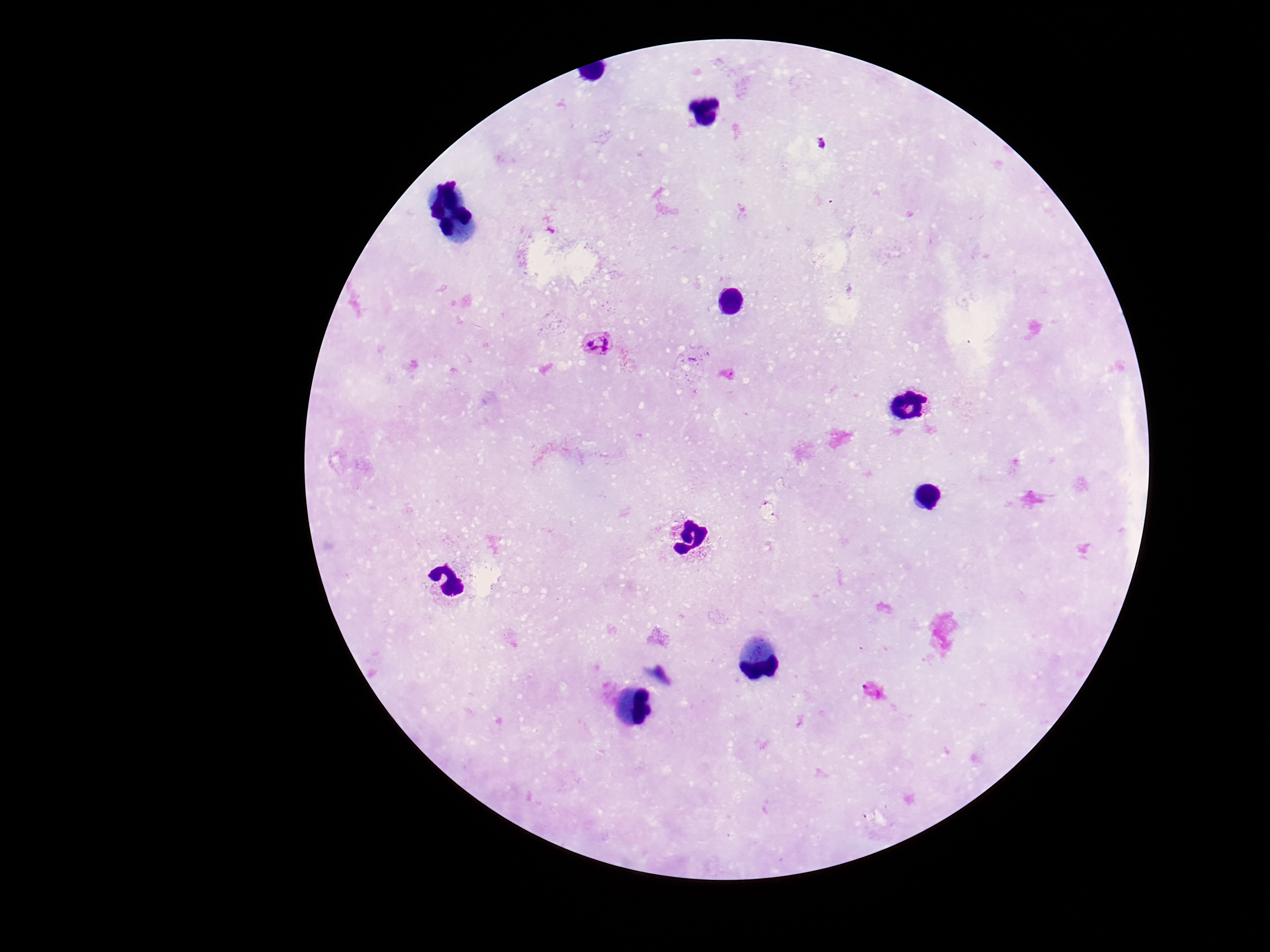
stain = Giemsa
Plasmodium parasite locations = approximate centers as [x, y] in pixels: [821, 143], [600, 343]
magnification = 100x
capture = smartphone camera through the microscope eyepiece
image size = 1270×952 pixels
preparation = thick blood smear
patient malaria status = positive
field of view = one from this slide